Give a bounding box for every leukocyte visible.
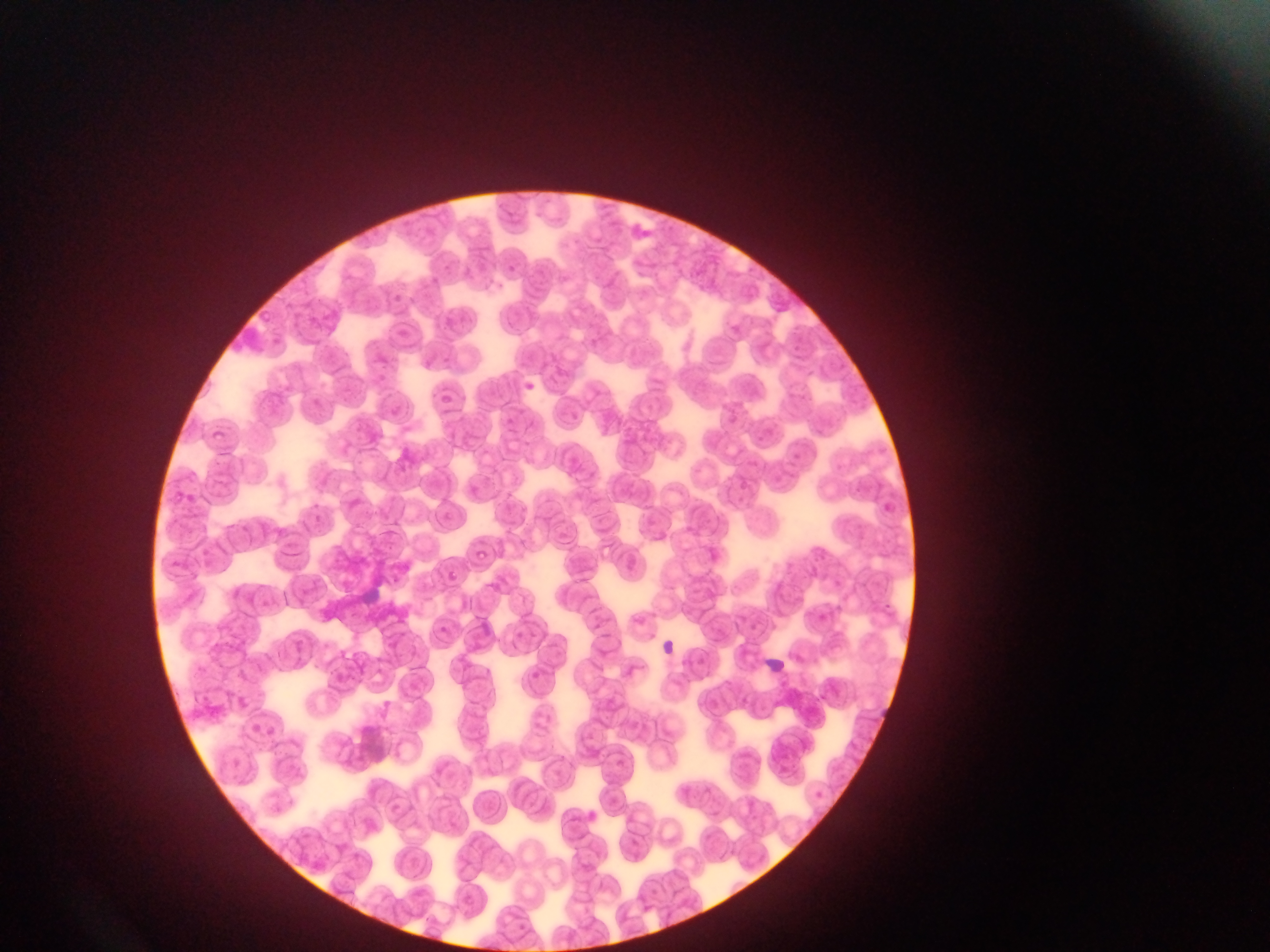
No leukocytes observed.

Approximate bounding boxes as [left, top, right, bottom] in pixels.
Summary:
  - Malaria parasite locations: [521, 379, 538, 394], [443, 568, 461, 586], [438, 622, 449, 632], [514, 626, 527, 642], [533, 669, 545, 679]
  - Field of view: single
  - Country: Ghana
  - Capture: mobile-phone photograph through a microscope
  - Image size: 1270×952 pixels
  - Preparation: thin blood film